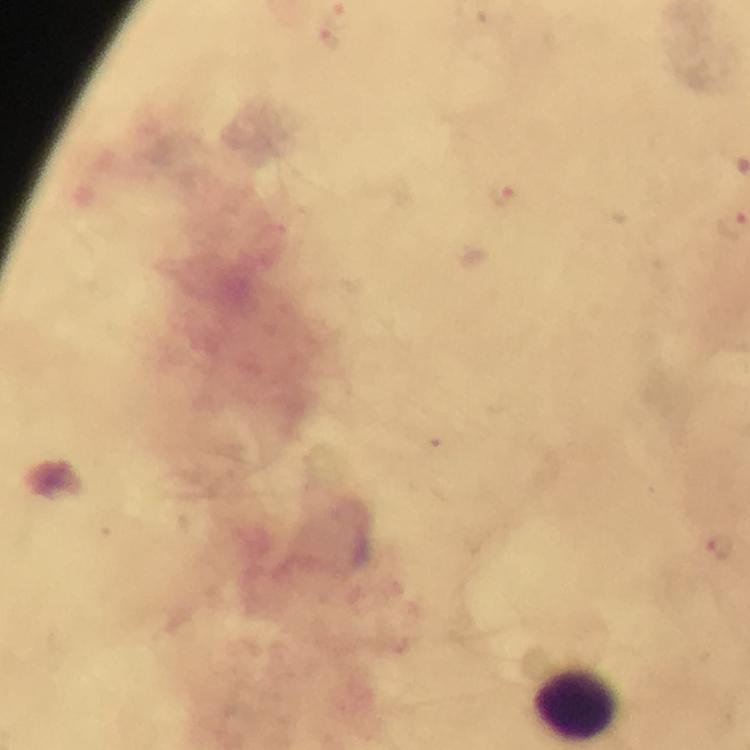

malaria_parasite_locations: 'approximate centers as (x, y) in pixels: (328, 40), (502, 191), (719, 546)'
stain: Giemsa
preparation: thick blood film
cropped_from: one field of view
immersion_oil: used
context: from a malaria diagnostic workup
magnification: 100x
capture: smartphone photograph through a microscope
image_size: 750×750 pixels